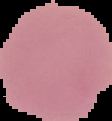
From a thin blood film. Image is 112×121 pixels. Malaria status: uninfected. Segmented cell region on a black background.